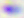 Toxoplasma gondii is shown. 400x magnification. Photomicrograph.